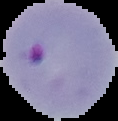
Malaria status: parasitized. From a thin blood film. Image is 118×121 pixels. Segmented cell region on a black background.